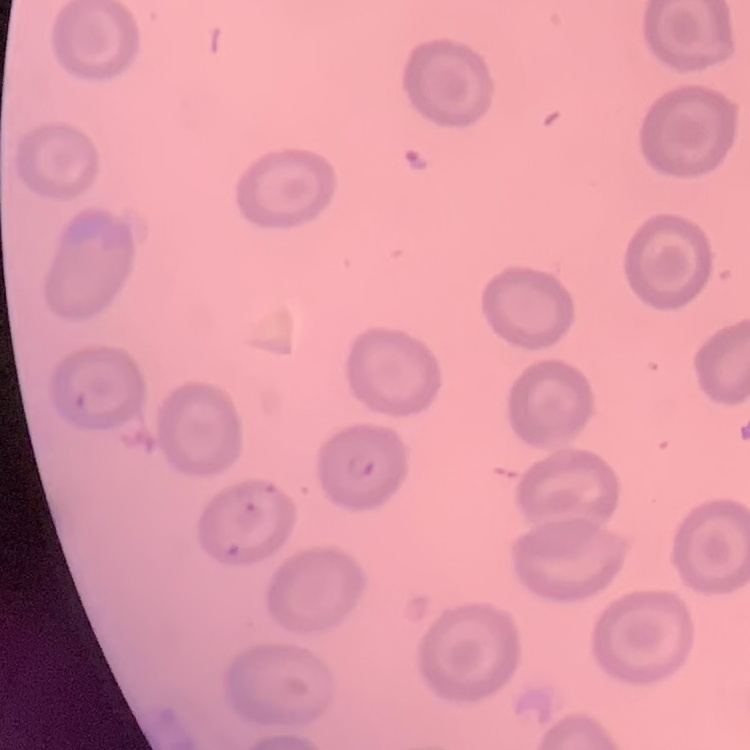 The red blood cells show no rouleaux formation. Field's or Giemsa stain. Thin blood film. Square crop of a larger photomicrograph.